Give the extent of all Plasmodium falciparum-infected red blood cells.
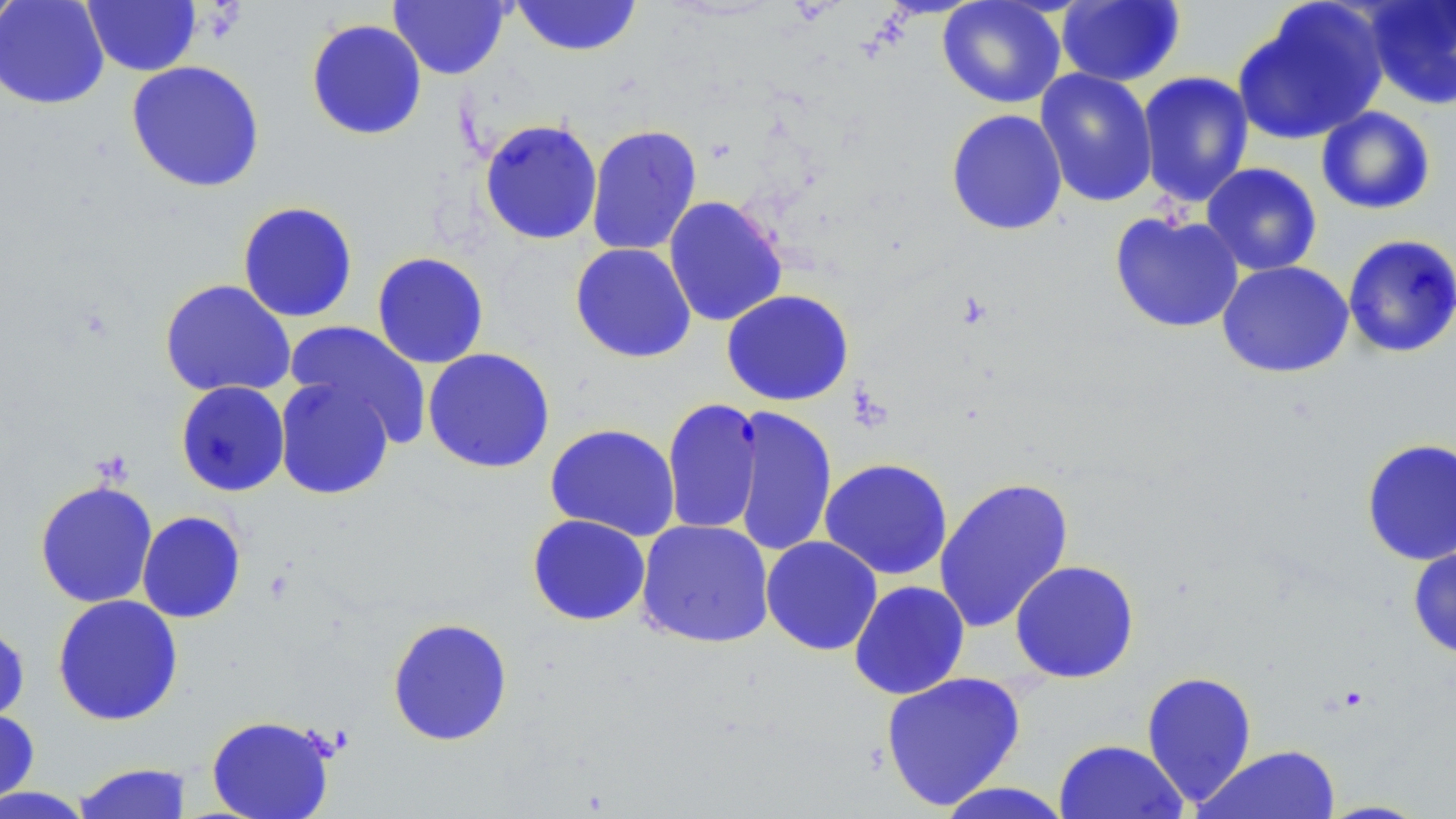

Approximate bounding boxes as [x1, y1, x2, y2] in pixels.
Plasmodium falciparum-infected red blood cells: [662, 398, 764, 536].

Uninfected red blood cell locations: [0, 0, 24, 33], [0, 0, 110, 110], [388, 0, 511, 80], [510, 0, 642, 57], [937, 0, 1067, 109], [82, 1, 201, 76], [1055, 1, 1186, 87], [1235, 1, 1389, 145], [1360, 1, 1456, 111], [306, 19, 427, 140], [126, 60, 265, 193], [1034, 68, 1159, 208], [1137, 71, 1255, 208], [1315, 106, 1437, 216], [945, 108, 1068, 236], [478, 118, 603, 245], [585, 124, 703, 257], [1200, 162, 1322, 276], [662, 196, 788, 327], [237, 201, 358, 323], [1108, 211, 1245, 334], [1342, 233, 1456, 358], [569, 243, 697, 363], [371, 251, 489, 369], [1216, 260, 1354, 379], [159, 279, 296, 399], [721, 289, 854, 406], [285, 320, 432, 446], [422, 348, 555, 474], [274, 378, 395, 500], [175, 381, 290, 497], [728, 405, 838, 558], [544, 423, 681, 541], [1360, 438, 1456, 566], [818, 458, 953, 580], [933, 476, 1075, 633], [34, 479, 158, 608], [136, 511, 247, 623], [527, 514, 651, 626], [635, 518, 775, 649], [760, 536, 883, 655], [1407, 541, 1456, 659], [1009, 559, 1140, 684], [848, 580, 970, 700], [52, 594, 184, 726], [387, 616, 513, 747], [0, 618, 30, 728], [1141, 669, 1258, 807], [879, 671, 1026, 811], [0, 708, 40, 806], [206, 715, 336, 819], [1053, 739, 1189, 819], [1195, 745, 1342, 819], [71, 761, 195, 818], [933, 781, 1077, 819], [0, 785, 97, 819]. Slide-level diagnosis: Plasmodium falciparum. May-Grünwald-Giemsa-stained preparation. Thin blood film. 1000x magnification. Optical microscopy. Image is 1456×819 pixels. One field of a larger specimen.